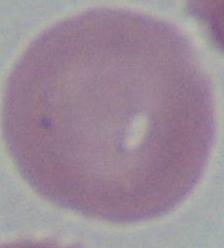
{
  "magnification": "1000x",
  "modality": "micrograph",
  "identification": "red blood cell"
}